State which parasite is depicted.
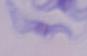
This is a trypanosome.

Micrograph. 1000x magnification.